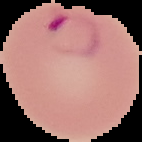
image_size: 142×142 pixels
preparation: thin blood smear
image_type: segmented cell region with the area outside set to black
result: malaria parasites identified